Name the parasite shown.
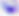

This is Toxoplasma gondii.

Photomicrograph. Captured at 400x magnification.